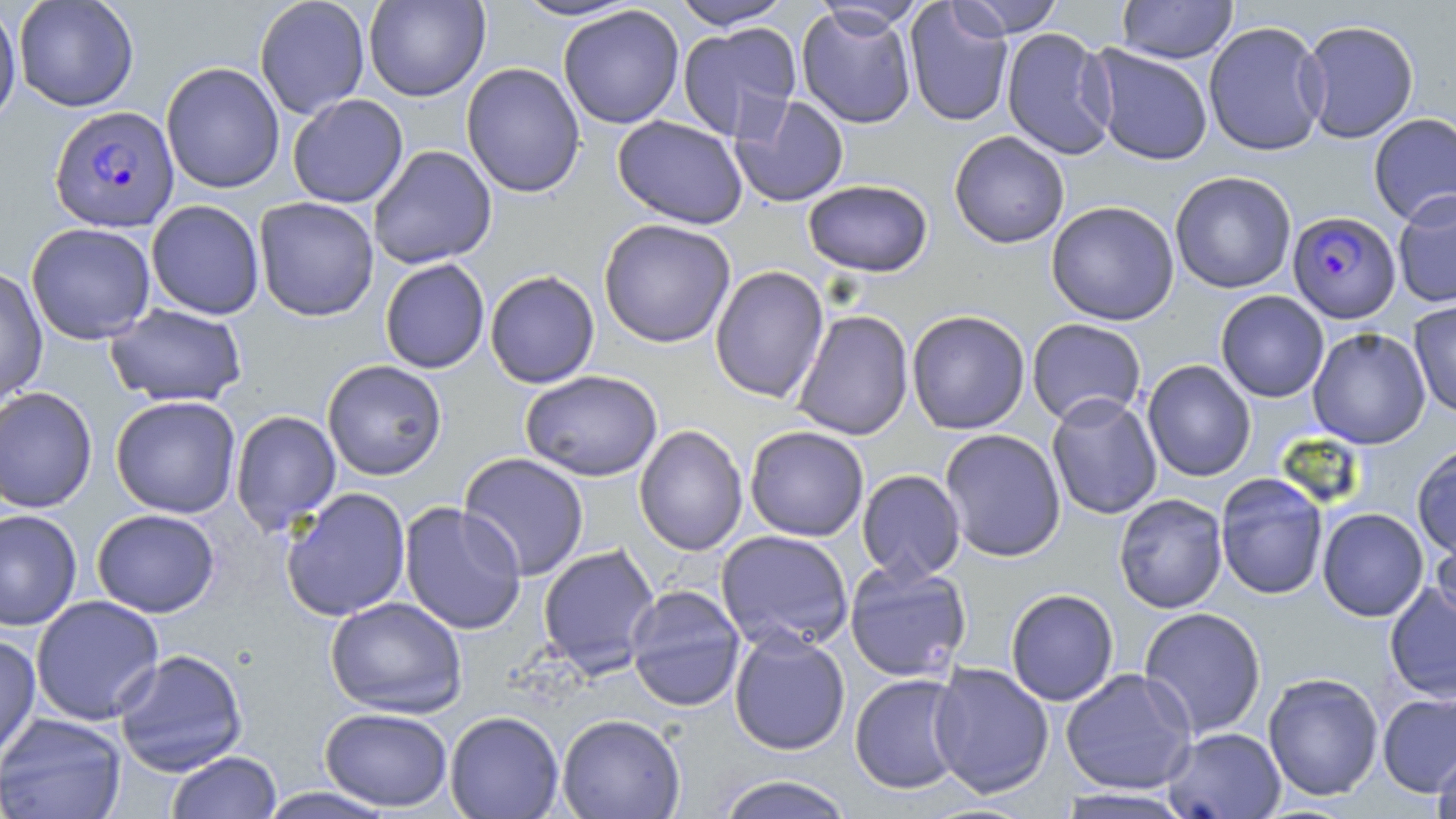

Approximate bounding boxes as (x1,y1)-(x2,y2) corner pairs in pixels. Plasmodium falciparum-infected red blood cell locations: (49,105)-(181,233), (1290,213)-(1403,325). Uninfected red blood cell locations: (0,0)-(21,130), (13,0)-(139,112), (254,0)-(371,119), (363,0)-(490,102), (510,0)-(643,22), (670,0)-(792,28), (948,0)-(1065,38), (1117,0)-(1238,64), (810,1)-(927,37), (904,2)-(1014,127), (558,5)-(685,129), (796,5)-(917,129), (1298,19)-(1420,143), (1204,21)-(1328,156), (677,22)-(801,141), (1001,27)-(1117,160), (1087,45)-(1214,166), (161,62)-(285,194), (461,62)-(586,199), (287,93)-(409,208), (730,95)-(849,207), (1368,113)-(1456,226), (612,115)-(748,229), (949,131)-(1070,248), (367,145)-(497,269), (1170,171)-(1296,294), (803,179)-(933,277), (1392,190)-(1456,308), (254,196)-(379,322), (146,199)-(265,320), (1046,200)-(1180,325), (598,218)-(736,348), (25,222)-(156,345), (379,258)-(490,374), (710,265)-(829,403), (0,266)-(48,405), (485,270)-(600,388), (1215,291)-(1329,402), (1408,299)-(1456,418), (105,303)-(249,407), (792,310)-(914,441), (906,310)-(1031,435), (1026,318)-(1148,426), (1307,327)-(1431,450), (321,359)-(448,481), (1142,359)-(1256,482), (520,370)-(663,482), (0,386)-(98,513), (1046,393)-(1162,520), (110,395)-(242,518), (230,410)-(342,536), (634,424)-(748,556), (744,425)-(869,541), (939,429)-(1066,562), (1411,441)-(1456,563), (458,452)-(589,581), (857,469)-(966,583), (1214,473)-(1329,600), (280,487)-(412,622), (1113,493)-(1228,613), (398,502)-(527,636), (0,508)-(83,632), (1317,508)-(1429,622), (91,509)-(220,617), (1431,523)-(1456,632), (716,529)-(854,652), (537,543)-(660,676), (844,561)-(972,683), (1384,581)-(1456,703), (625,584)-(745,711), (1005,589)-(1119,706), (30,595)-(165,725), (325,596)-(468,718), (1138,606)-(1267,739), (729,630)-(851,755), (0,634)-(41,764), (112,648)-(248,776), (928,662)-(1054,798), (1060,668)-(1197,795), (1262,672)-(1384,801), (849,673)-(968,795), (1377,690)-(1456,798), (320,707)-(453,811), (445,711)-(564,818), (0,712)-(128,819), (556,713)-(686,819), (1162,727)-(1285,818), (1431,746)-(1456,819), (166,751)-(282,818), (714,774)-(856,819), (254,787)-(399,818), (1053,788)-(1198,818). Slide-level diagnosis: Plasmodium falciparum. Single field of view. Captured at 1000x magnification. Image is 1456×819 pixels. May-Grünwald-Giemsa-stained preparation. Optical microscopy. Thin blood smear.